Assess this cell for malaria.
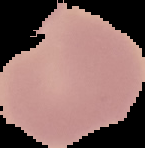

Uninfected.

Segmented cell region on a black background. Image is 145×148 pixels. From a thin blood smear.